Assess this cell for malaria.
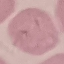
It is uninfected.

Acquired by smartphone through the microscope eyepiece. Automatically extracted cell patch, resized to 64 × 64 pixels. Giemsa stain. Thin blood smear.